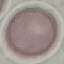 Result: negative for malaria parasites. Automatically extracted cell patch, resized to 64 × 64 pixels. Giemsa stain. Thin blood smear. Acquired by smartphone through the microscope eyepiece.